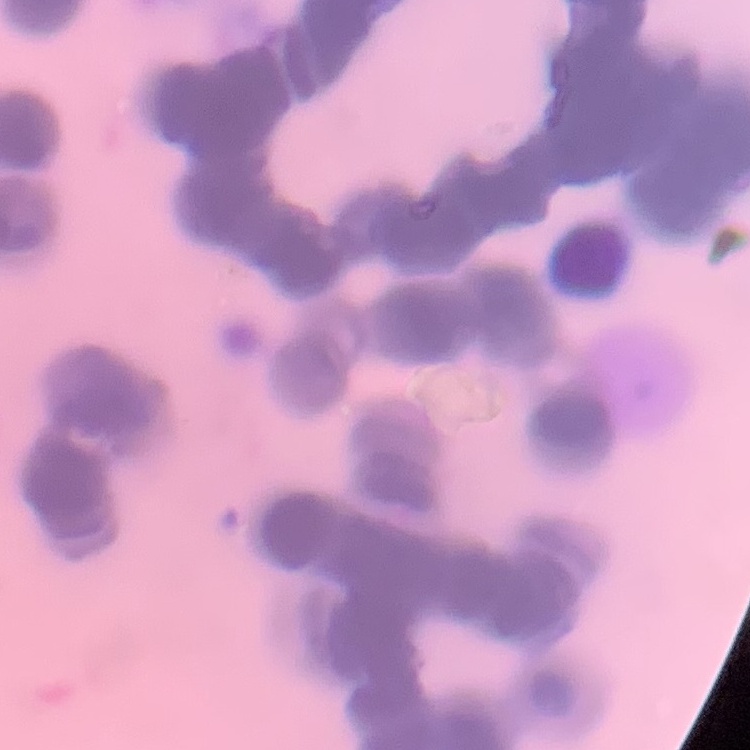

The red blood cells show rouleaux formation. Thin peripheral smear. Stained with either Field's or Giemsa. One tile cut from a larger photomicrograph.